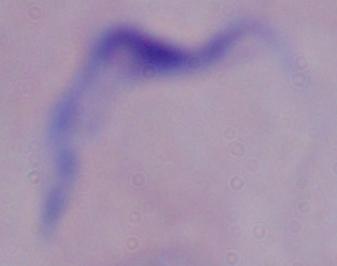
modality: photomicrograph
magnification: 1000x
identification: trypanosome